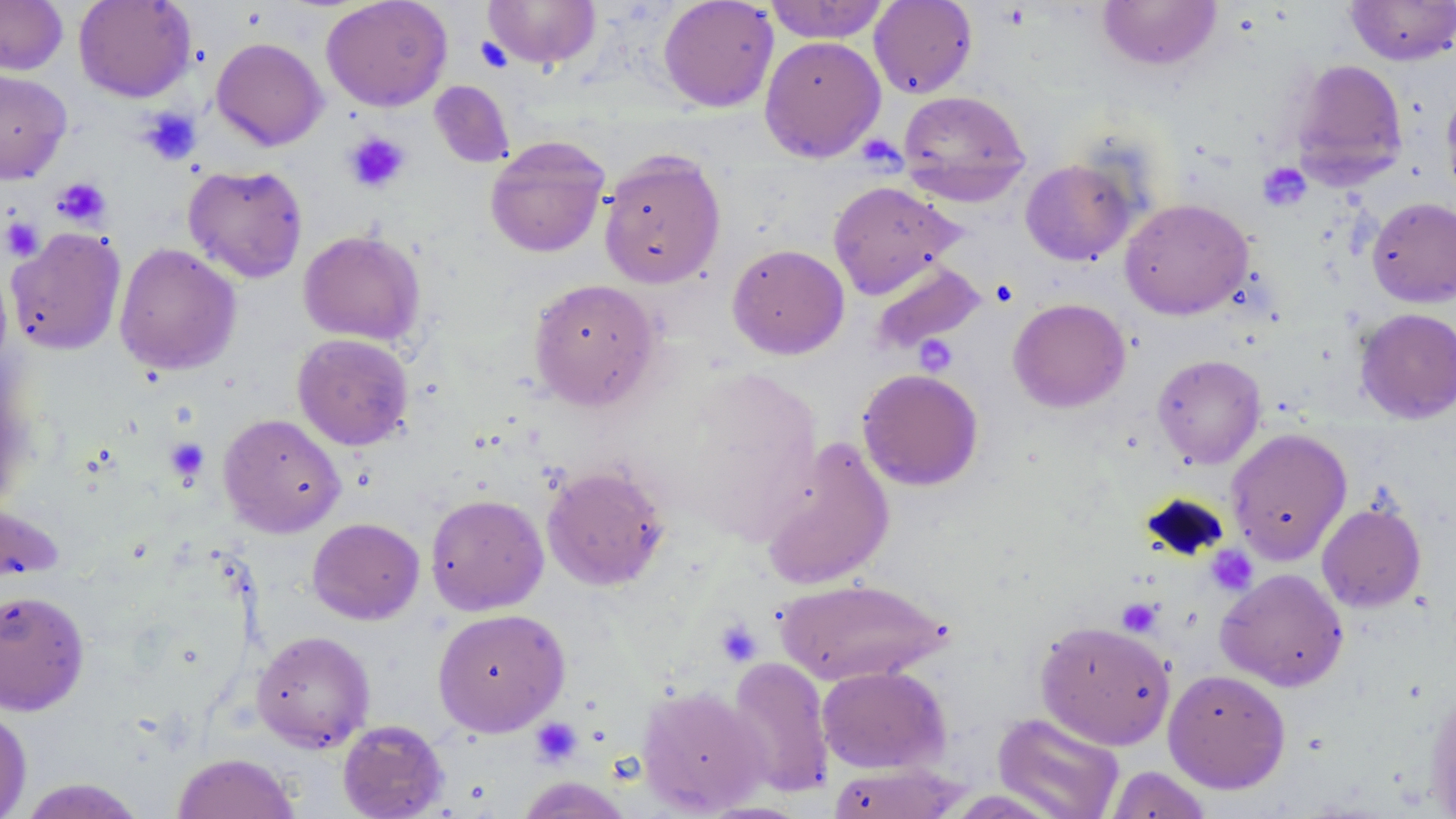

Summary:
  - Coordinate format: approximate bounding boxes as named x1/y1/x2/y2 corners in pixels
  - Platelet locations: (x1=475, y1=37, x2=512, y2=73), (x1=138, y1=107, x2=202, y2=166), (x1=343, y1=131, x2=411, y2=193), (x1=1258, y1=163, x2=1311, y2=211), (x1=51, y1=177, x2=111, y2=228), (x1=1, y1=217, x2=44, y2=261), (x1=165, y1=438, x2=210, y2=482), (x1=1207, y1=545, x2=1258, y2=596), (x1=1116, y1=598, x2=1162, y2=636), (x1=715, y1=620, x2=762, y2=667), (x1=530, y1=717, x2=582, y2=767)
  - Uninfected red blood cell locations: (x1=0, y1=0, x2=68, y2=76), (x1=73, y1=0, x2=197, y2=102), (x1=321, y1=0, x2=453, y2=111), (x1=483, y1=0, x2=601, y2=69), (x1=658, y1=0, x2=779, y2=112), (x1=763, y1=0, x2=890, y2=43), (x1=869, y1=0, x2=978, y2=99), (x1=1097, y1=0, x2=1222, y2=71), (x1=1345, y1=1, x2=1455, y2=66), (x1=759, y1=35, x2=886, y2=162), (x1=211, y1=37, x2=327, y2=151), (x1=1289, y1=59, x2=1408, y2=187), (x1=0, y1=69, x2=72, y2=184), (x1=429, y1=81, x2=515, y2=168), (x1=1441, y1=87, x2=1456, y2=201), (x1=897, y1=90, x2=1031, y2=202), (x1=484, y1=135, x2=610, y2=258), (x1=598, y1=149, x2=726, y2=289), (x1=1020, y1=158, x2=1137, y2=266), (x1=183, y1=164, x2=308, y2=283), (x1=827, y1=180, x2=962, y2=299), (x1=1119, y1=197, x2=1253, y2=320), (x1=1366, y1=197, x2=1456, y2=307), (x1=6, y1=227, x2=126, y2=355), (x1=299, y1=230, x2=426, y2=346), (x1=114, y1=243, x2=241, y2=375), (x1=727, y1=244, x2=850, y2=359), (x1=869, y1=259, x2=986, y2=353), (x1=528, y1=278, x2=662, y2=410), (x1=1007, y1=298, x2=1131, y2=413), (x1=1354, y1=307, x2=1456, y2=424), (x1=292, y1=333, x2=414, y2=450), (x1=1152, y1=354, x2=1266, y2=469), (x1=857, y1=368, x2=984, y2=491), (x1=218, y1=413, x2=345, y2=537), (x1=1225, y1=428, x2=1352, y2=564), (x1=758, y1=438, x2=895, y2=590), (x1=541, y1=464, x2=671, y2=591), (x1=425, y1=487, x2=670, y2=602), (x1=425, y1=493, x2=549, y2=615), (x1=1, y1=494, x2=65, y2=589), (x1=1317, y1=500, x2=1427, y2=612), (x1=307, y1=517, x2=425, y2=624), (x1=1216, y1=568, x2=1348, y2=691), (x1=774, y1=578, x2=949, y2=686), (x1=0, y1=589, x2=90, y2=715), (x1=432, y1=608, x2=570, y2=736), (x1=1034, y1=619, x2=1176, y2=750), (x1=251, y1=630, x2=375, y2=751), (x1=725, y1=656, x2=835, y2=798), (x1=816, y1=665, x2=950, y2=774), (x1=1162, y1=668, x2=1292, y2=793), (x1=1425, y1=682, x2=1456, y2=818), (x1=637, y1=685, x2=769, y2=815), (x1=0, y1=702, x2=32, y2=819), (x1=993, y1=712, x2=1125, y2=819), (x1=337, y1=719, x2=449, y2=818), (x1=171, y1=752, x2=300, y2=819), (x1=825, y1=762, x2=968, y2=818), (x1=1104, y1=765, x2=1214, y2=818), (x1=515, y1=777, x2=635, y2=818), (x1=16, y1=778, x2=148, y2=818)
  - Slide-level diagnosis: no evidence of blood parasites
  - Magnification: 1000x
  - Modality: optical microscopy
  - Field of view: one of a larger specimen
  - Preparation: thin blood film
  - Image size: 1456×819 pixels
  - Stain: May-Grünwald-Giemsa